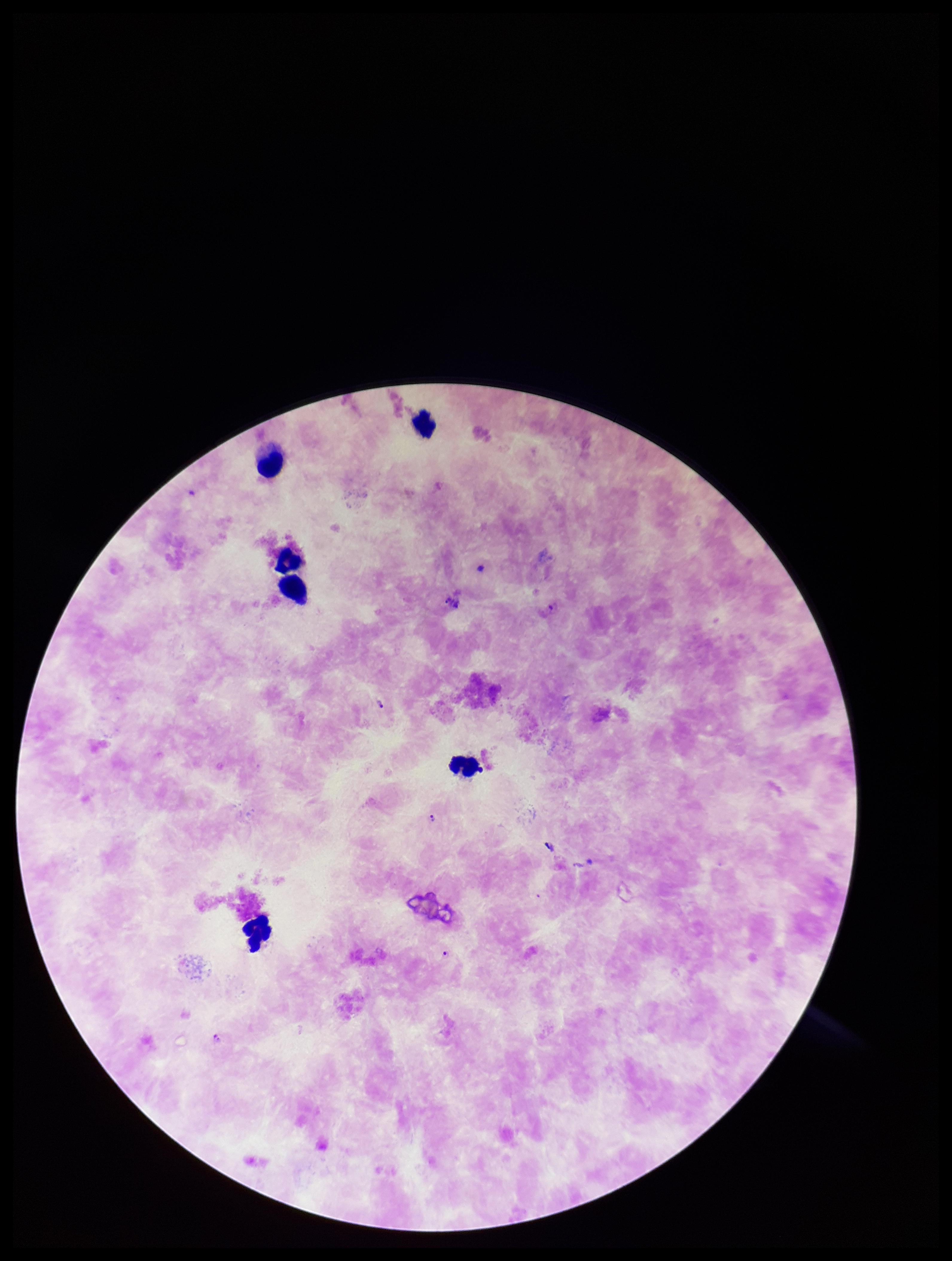

{
  "stain": "Giemsa",
  "leukocyte_count": 6,
  "patient_malaria_status": "positive",
  "image_size": "952×1261 pixels",
  "field_of_view": "single",
  "capture": "smartphone photograph through the microscope eyepiece",
  "parasite_count": 3,
  "species_reported_for_this_patient": "Plasmodium falciparum",
  "preparation": "thick smear",
  "plasmodium_parasites": "identified"
}